Assess this cell for malaria.
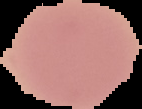
It is uninfected.

The area outside the segmented cell region is set to black. Image is 142×109 pixels. From a thin blood smear.